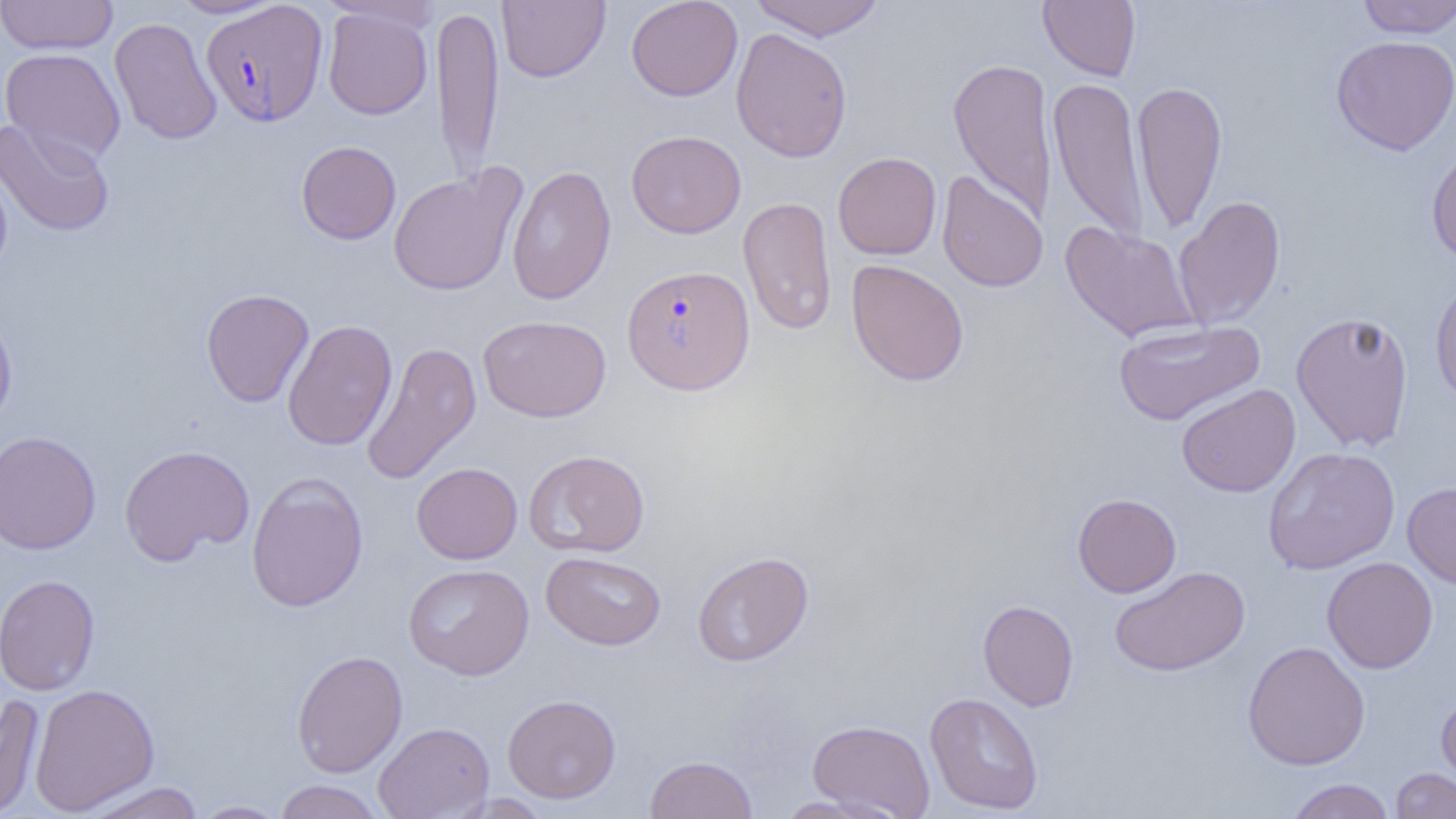
Summary:
  - Coordinate format: approximate bounding boxes as (x1,y1)-(x2,y2) corner pairs in pixels
  - Uninfected red blood cell locations: (0,0)-(118,55), (168,0)-(283,18), (497,0)-(610,82), (626,0)-(743,101), (749,0)-(886,41), (1038,0)-(1141,81), (1355,0)-(1456,38), (431,3)-(504,179), (323,7)-(433,119), (110,17)-(222,145), (730,26)-(852,162), (1331,35)-(1456,155), (1,47)-(126,166), (947,57)-(1057,222), (1048,75)-(1150,245), (1132,80)-(1228,235), (0,119)-(114,237), (626,130)-(746,238), (296,140)-(401,245), (1426,143)-(1456,265), (833,152)-(942,259), (0,159)-(13,278), (506,164)-(617,305), (388,166)-(526,296), (936,170)-(1048,292), (1173,195)-(1286,329), (737,196)-(837,336), (1060,221)-(1199,343), (846,259)-(969,386), (1430,274)-(1456,407), (201,288)-(314,407), (0,309)-(17,430), (1290,310)-(1415,452), (479,315)-(611,422), (282,319)-(397,451), (1113,320)-(1264,426), (361,341)-(482,485), (1176,383)-(1300,498), (0,430)-(102,555), (119,443)-(255,565), (1263,446)-(1401,574), (523,449)-(650,557), (412,462)-(523,564), (246,473)-(368,612), (1402,481)-(1456,590), (1072,493)-(1181,598), (692,550)-(814,666), (541,551)-(667,650), (1322,556)-(1438,673), (404,563)-(534,680), (1109,565)-(1250,677), (0,574)-(100,696), (978,599)-(1079,711), (1242,641)-(1370,770), (292,649)-(408,778), (29,683)-(159,815), (1436,690)-(1456,795), (925,692)-(1044,815), (0,694)-(45,817), (503,694)-(621,803), (807,719)-(935,818), (373,721)-(495,819), (644,754)-(758,818), (1390,768)-(1456,819), (1285,779)-(1395,819), (273,780)-(386,819), (79,781)-(205,819), (771,795)-(897,818), (190,800)-(288,818)
  - Plasmodium falciparum-infected red blood cell locations: (201,1)-(328,127), (622,264)-(755,395)
  - Slide-level diagnosis: Plasmodium falciparum
  - Magnification: 1000x
  - Image size: 1456×819 pixels
  - Preparation: thin blood film
  - Field of view: single
  - Modality: optical microscopy